Classify this cell by malaria status.
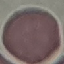
It is uninfected.

Summary:
  - Preparation: thin blood smear
  - Capture: smartphone through the microscope eyepiece
  - Stain: Giemsa
  - Image type: cell patch, automatically extracted from a larger field of view and resized to 64 × 64 pixels